State which cell type is depicted.
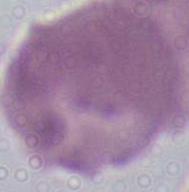
An erythrocyte.

Micrograph. Captured at 1000x magnification.